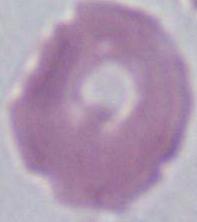
An erythrocyte is seen. Captured at 1000x magnification. Micrograph.